Identify the parasite.
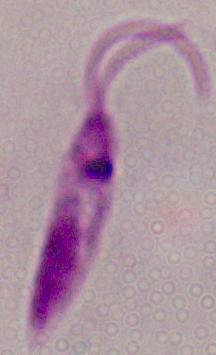

This is Leishmania.

magnification: 1000x
modality: photomicrograph